Classify this cell by malaria status.
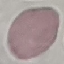

It is uninfected.

Summary:
  - Capture: smartphone camera at the microscope eyepiece
  - Stain: Giemsa
  - Preparation: thin blood film
  - Image type: cell patch, automatically extracted from a larger field of view and resized to 64 × 64 pixels